Assess this cell for malaria.
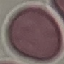
It is uninfected.

capture = smartphone through the microscope eyepiece
image type = automatically extracted cell patch, resized to 64 × 64 pixels
preparation = thin blood film
stain = Giemsa